Name the parasite shown.
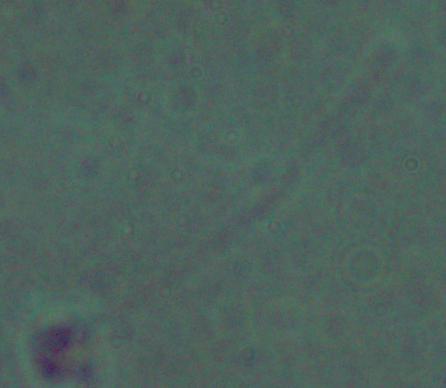

This is Leishmania.

Micrograph. Captured at 1000x magnification.